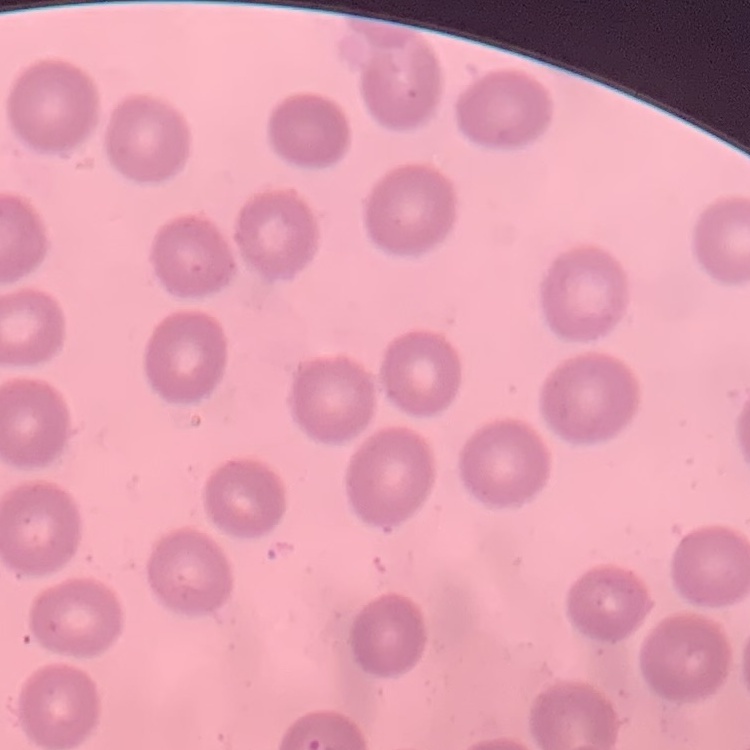

The erythrocytes show no rouleaux formation. Field's or Giemsa stain. Square crop of a larger photomicrograph. Thin peripheral smear.